Outline each uninfected red blood cell.
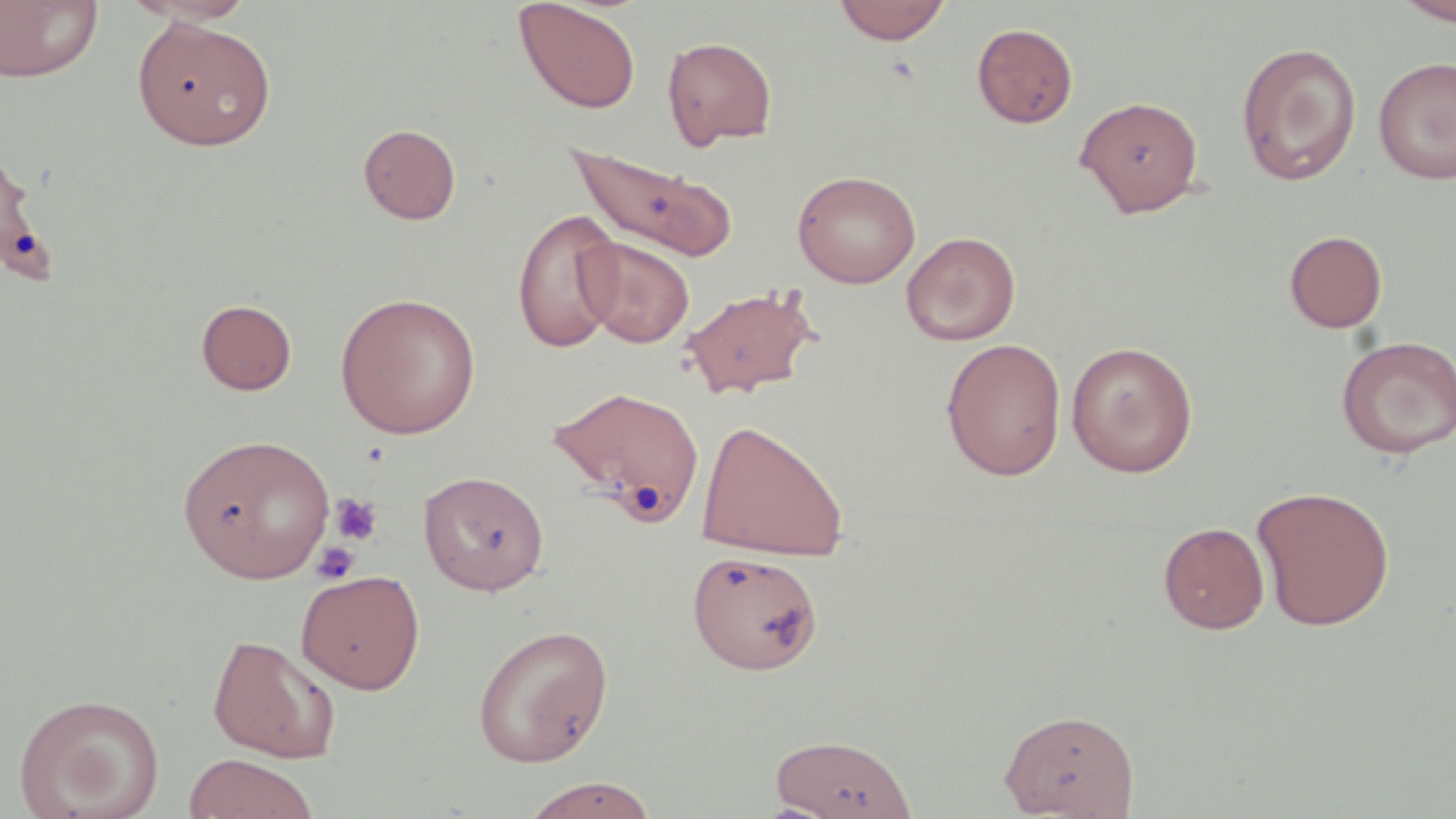

Approximate bounding boxes as (x1,y1)-(x2,y2) corner pairs in pixels.
Uninfected red blood cells: (0,0)-(103,84), (123,0)-(259,26), (513,0)-(642,115), (833,0)-(951,45), (1394,0)-(1456,26), (132,16)-(277,150), (972,22)-(1078,128), (662,36)-(777,148), (1235,42)-(1362,185), (1373,57)-(1456,184), (1074,96)-(1204,217), (358,123)-(461,224), (0,142)-(52,287), (565,143)-(738,263), (792,170)-(921,288), (512,208)-(624,354), (1284,230)-(1387,333), (901,231)-(1021,345), (577,238)-(695,348), (680,284)-(820,400), (335,292)-(481,439), (196,299)-(297,395), (1335,335)-(1455,460), (941,337)-(1067,480), (1065,340)-(1198,476), (550,384)-(707,525), (696,418)-(849,562), (177,434)-(335,584), (418,470)-(549,596), (1252,485)-(1395,631), (1158,522)-(1270,634), (687,549)-(822,675), (295,569)-(425,693), (472,623)-(614,768), (206,633)-(341,762), (14,692)-(165,819), (998,708)-(1140,818), (769,732)-(916,818), (182,753)-(318,819), (519,777)-(661,818).

Summary:
  - Platelet locations: (330,493)-(383,545), (311,541)-(361,584)
  - Slide-level diagnosis: negative for blood parasites
  - Preparation: thin blood film
  - Stain: May-Grünwald-Giemsa
  - Image size: 1456×819 pixels
  - Field of view: one of a larger specimen
  - Modality: light microscopy
  - Magnification: 1000x